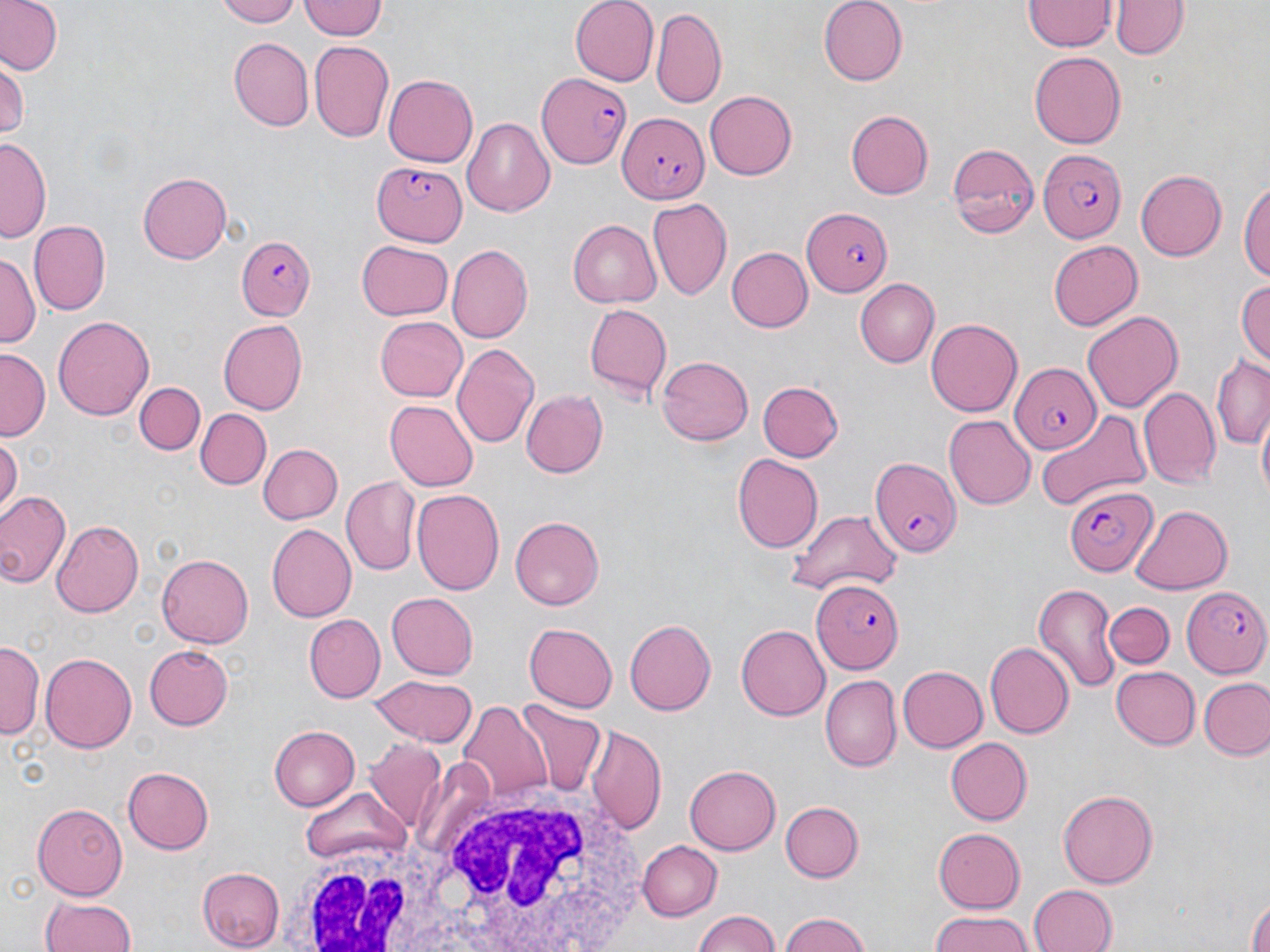
Summary:
  - Coordinate format: approximate bounding boxes as [x1, y1, x2, y2] in pixels
  - Plasmodium falciparum-infected red blood cell locations: [532, 68, 631, 173], [617, 111, 704, 205], [1038, 148, 1127, 242], [370, 163, 466, 246], [802, 208, 893, 296], [234, 235, 317, 322], [1008, 361, 1101, 455], [869, 455, 959, 553], [1063, 483, 1157, 576], [811, 579, 904, 674], [1184, 585, 1270, 679]
  - White blood cell locations: [406, 779, 662, 951], [275, 838, 443, 951]
  - Uninfected red blood cell locations: [0, 0, 62, 76], [215, 0, 305, 26], [297, 0, 386, 41], [568, 0, 658, 86], [817, 0, 909, 85], [1026, 1, 1116, 51], [1112, 2, 1188, 59], [651, 10, 727, 110], [230, 37, 313, 131], [310, 42, 394, 143], [1029, 49, 1127, 147], [0, 63, 25, 140], [384, 74, 479, 166], [706, 91, 798, 180], [845, 109, 934, 199], [462, 116, 554, 217], [0, 137, 49, 245], [947, 144, 1038, 237], [1135, 168, 1227, 262], [138, 172, 232, 264], [1241, 176, 1269, 289], [647, 198, 733, 302], [27, 219, 112, 315], [567, 220, 660, 308], [356, 240, 453, 322], [1048, 241, 1144, 330], [446, 244, 533, 343], [725, 247, 812, 332], [1, 250, 40, 346], [854, 278, 939, 367], [1234, 278, 1270, 370], [582, 302, 671, 398], [1082, 311, 1183, 413], [52, 313, 154, 419], [373, 315, 468, 403], [926, 318, 1024, 417], [216, 319, 306, 413], [452, 343, 540, 449], [1, 348, 48, 440], [657, 356, 752, 446], [1209, 357, 1270, 448], [757, 381, 844, 462], [134, 382, 204, 455], [1139, 387, 1221, 490], [520, 389, 607, 479], [385, 400, 479, 491], [196, 410, 270, 489], [1036, 411, 1151, 514], [1256, 415, 1269, 503], [944, 416, 1034, 508], [0, 434, 22, 513], [256, 444, 343, 525], [734, 453, 823, 552], [342, 475, 420, 576], [411, 489, 504, 595], [0, 490, 71, 590], [1131, 504, 1232, 596], [788, 510, 901, 596], [512, 515, 608, 611], [50, 520, 144, 617], [266, 523, 354, 621], [157, 554, 254, 648], [1033, 582, 1121, 693], [385, 593, 479, 679], [1105, 603, 1173, 669], [305, 614, 385, 702], [624, 618, 717, 714], [523, 620, 617, 713], [737, 625, 830, 720], [0, 643, 40, 738], [985, 643, 1072, 739], [143, 645, 234, 730], [42, 651, 137, 752], [896, 665, 988, 753], [1110, 666, 1200, 748], [368, 676, 477, 745], [820, 677, 901, 772], [1200, 677, 1270, 759], [456, 700, 553, 802], [519, 703, 606, 797], [267, 724, 359, 812], [589, 726, 666, 833], [946, 738, 1032, 825], [362, 741, 448, 832], [683, 765, 781, 855], [122, 766, 212, 854], [301, 790, 411, 868], [1057, 791, 1157, 889], [779, 801, 861, 883], [35, 802, 128, 901], [932, 827, 1025, 913], [638, 840, 720, 918], [1038, 840, 1144, 952], [198, 868, 284, 948], [1026, 884, 1118, 952], [38, 894, 137, 952], [1247, 898, 1269, 952], [690, 910, 787, 952], [777, 911, 875, 952], [925, 912, 1038, 952]
  - Slide-level diagnosis: Plasmodium falciparum
  - Field of view: one of a larger specimen
  - Magnification: 1000x
  - Preparation: thin blood smear
  - Stain: May-Grünwald-Giemsa
  - Modality: light microscopy
  - Image size: 1270×952 pixels